Classify this cell by malaria status.
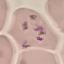
It is parasitized.

Photographed with a smartphone camera at the microscope eyepiece. Giemsa stain. Thin smear of blood. Cell patch, automatically extracted from a larger field of view and resized to 64 × 64 pixels.